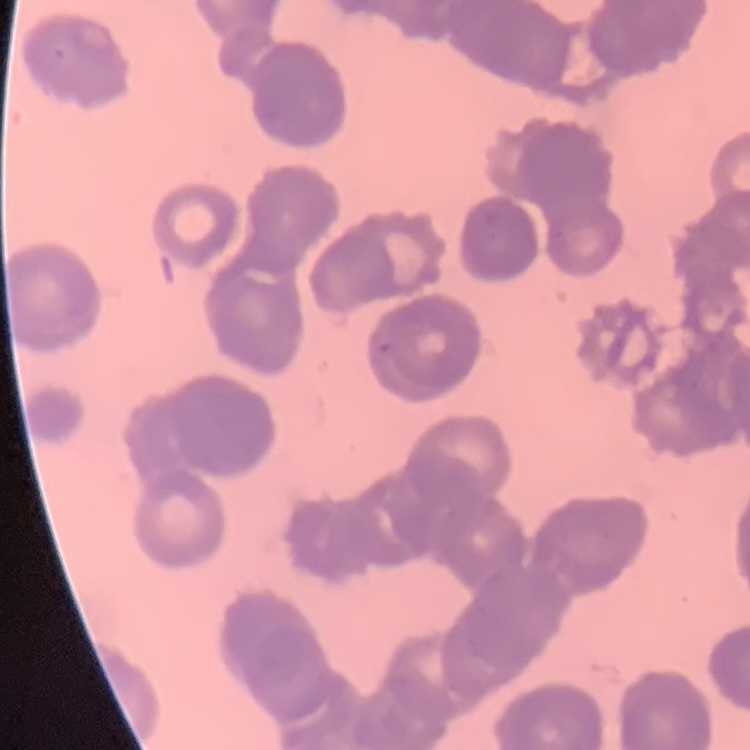
Summary:
  - Erythrocyte morphology: rouleaux formation
  - Image type: one tile cut from a larger photomicrograph
  - Preparation: thin blood film
  - Stain: Field's or Giemsa